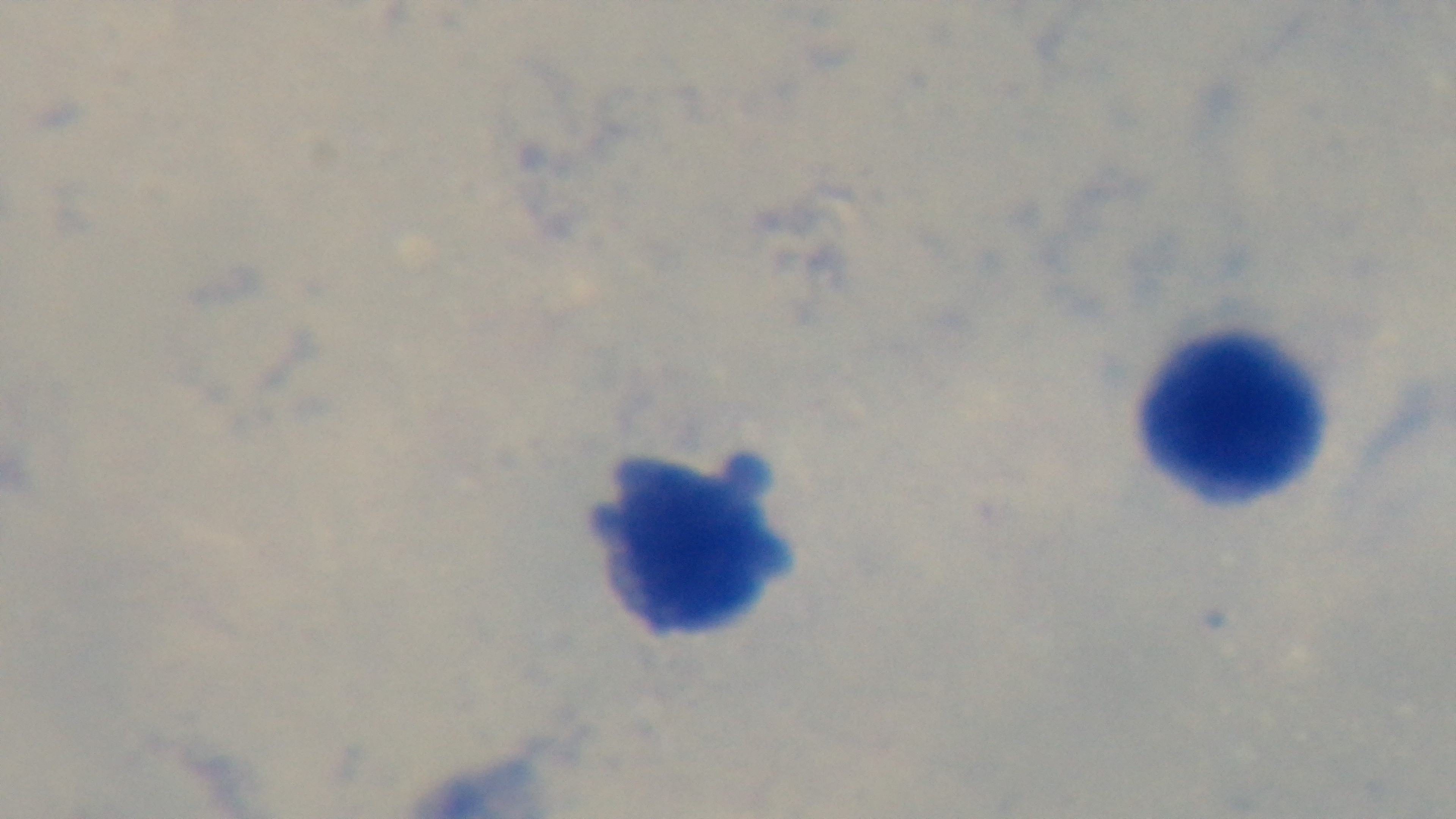
field of view = one from the slide
capture = mounted 4K digital camera
objective = 100x oil immersion
modality = light microscopy
stain = Giemsa
malaria status = uninfected
preparation = thick blood film